Name the parasite shown.
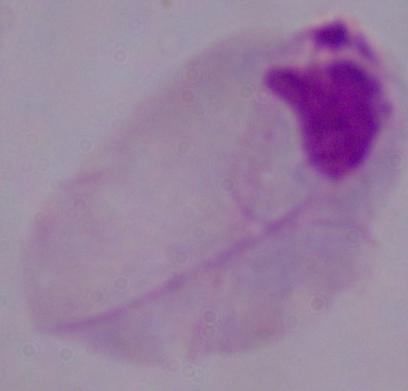

A trichomonad.

modality: micrograph
magnification: 1000x